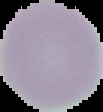 Cell region segmented out of the field of view; the surrounding area is masked to black. Result: negative for malaria parasites. From a thin blood film. Image is 103×112 pixels.